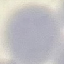
result: no malaria parasites detected
image_type: cell patch, automatically extracted from a larger field of view and resized to 64 × 64 pixels
preparation: thin blood smear
stain: Giemsa
capture: smartphone through the microscope eyepiece